Comment on the morphology of the erythrocytes.
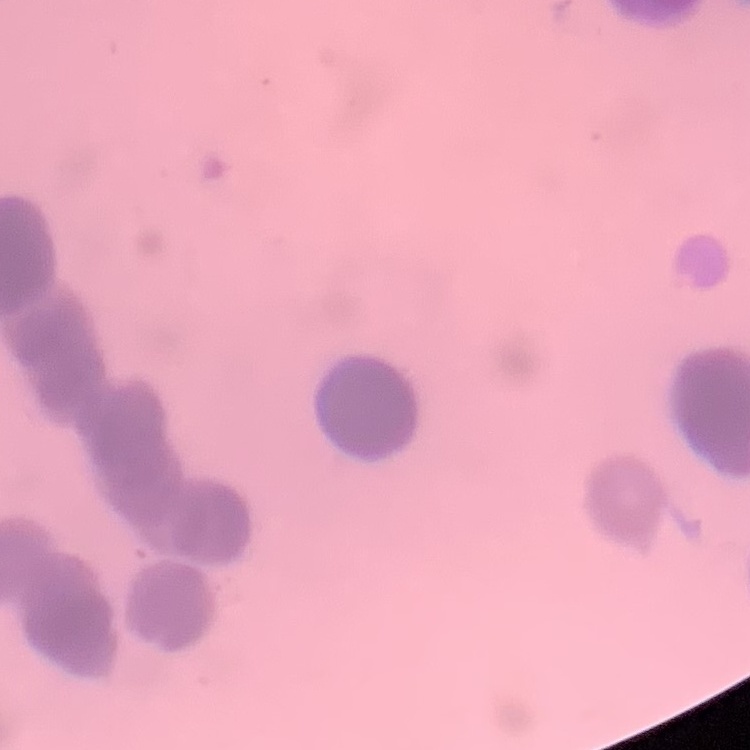
Rouleaux formation.

Stained with either Field's or Giemsa. Thin peripheral smear. Square crop of a larger photomicrograph.